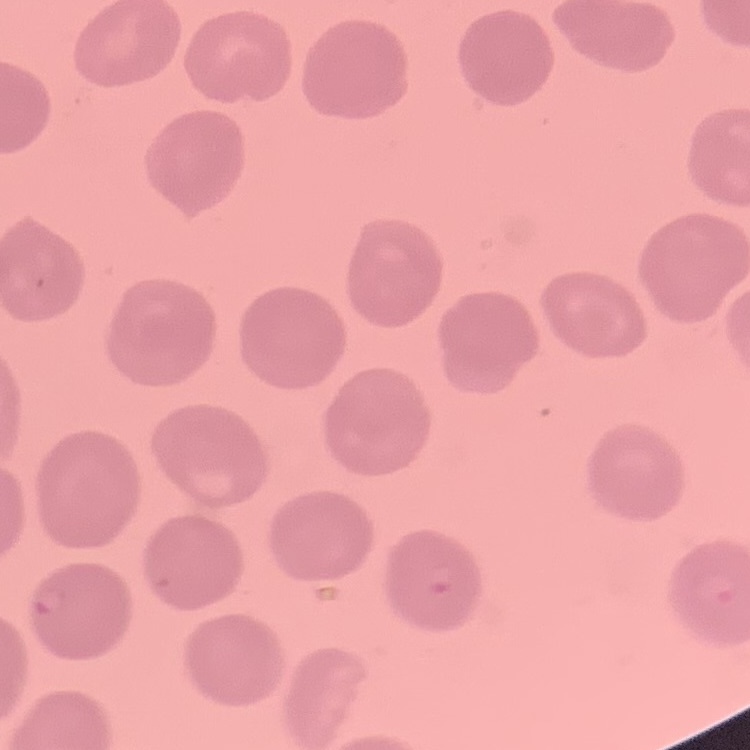
Summary:
  - Erythrocyte morphology: no rouleaux formation
  - Stain: Field's or Giemsa
  - Preparation: thin blood film
  - Image type: square crop of a larger photomicrograph